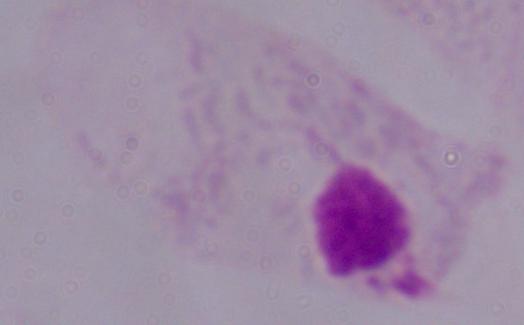

magnification = 1000x
identification = trichomonad
modality = micrograph